Name the parasite shown.
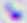
This is Toxoplasma gondii.

Captured at 400x magnification. Photomicrograph.